Assess the morphology of the red blood cells.
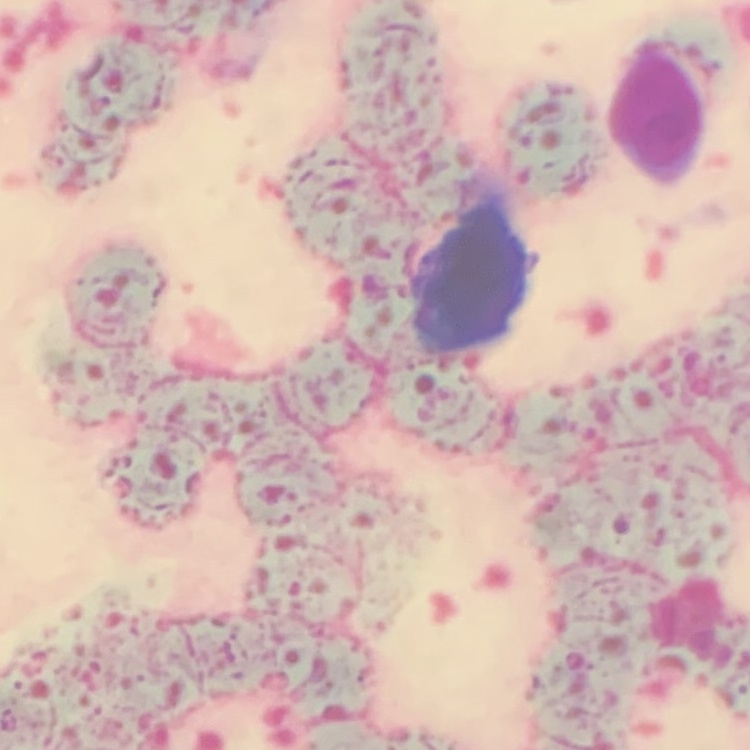

They show rouleaux formation.

image_type: square crop of a larger photomicrograph
stain: Field's or Giemsa
preparation: thin peripheral smear